Report the malaria status of this cell.
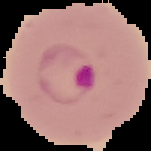
Parasitized.

Cell region segmented out of the field of view; the surrounding area is masked to black. Image is 151×151 pixels. From a thin blood film.